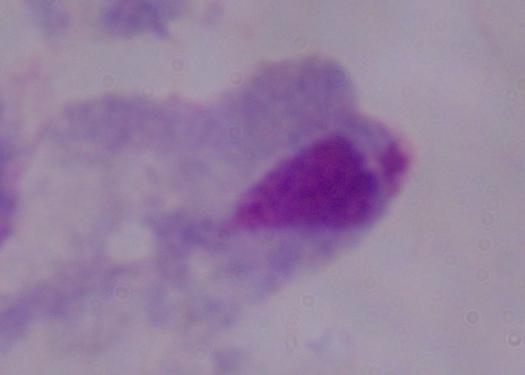
Summary:
  - Modality: micrograph
  - Identification: trichomonad
  - Magnification: 1000x